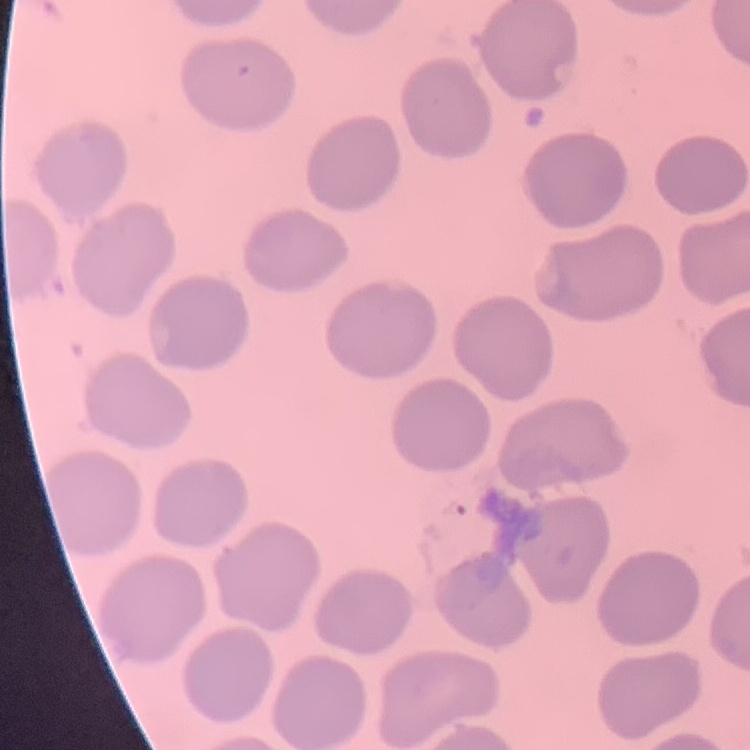

erythrocyte morphology = no rouleaux formation
preparation = thin blood film
image type = square crop of a larger photomicrograph
stain = Field's or Giemsa